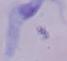
modality = photomicrograph
identification = trypanosome
magnification = 1000x